Assess this cell for malaria.
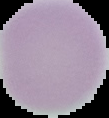

Uninfected.

Summary:
  - Preparation: thin blood smear
  - Image size: 109×118 pixels
  - Image type: segmented cell region with the area outside set to black